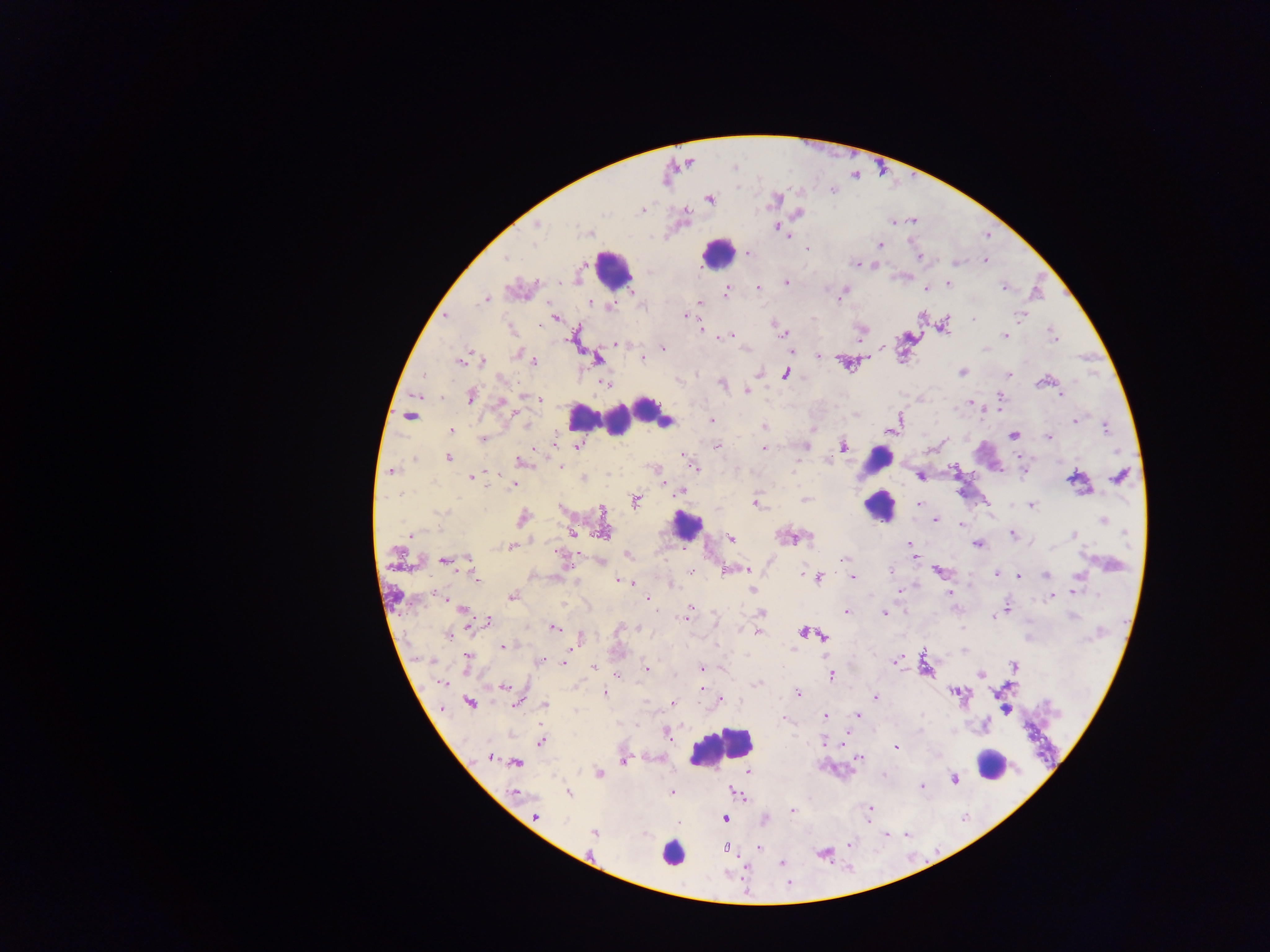
Approximate centers as {x, y} in pixels. Malaria parasite locations: {709, 199}, {774, 201}, {641, 211}, {798, 213}, {537, 225}, {778, 229}, {589, 233}, {880, 244}, {807, 248}, {748, 254}, {919, 257}, {506, 258}, {986, 260}, {856, 263}, {786, 283}, {949, 284}, {1003, 286}, {758, 288}, {926, 288}, {725, 291}, {841, 293}, {486, 300}, {701, 302}, {592, 303}, {611, 306}, {686, 315}, {1019, 316}, {554, 318}, {973, 319}, {944, 325}, {700, 329}, {778, 329}, {782, 333}, {1053, 334}, {729, 335}, {1005, 335}, {618, 344}, {882, 347}, {663, 349}, {985, 349}, {518, 354}, {819, 356}, {529, 358}, {642, 358}, {597, 359}, {481, 360}, {460, 361}, {534, 361}, {962, 372}, {758, 374}, {1009, 374}, {425, 375}, {786, 375}, {501, 379}, {1042, 381}, {605, 383}, {722, 384}, {748, 390}, {1061, 394}, {471, 396}, {532, 397}, {999, 397}, {539, 399}, {501, 402}, {971, 402}, {899, 418}, {713, 420}, {1076, 421}, {665, 423}, {896, 423}, {527, 424}, {764, 427}, {1105, 427}, {451, 430}, {1013, 435}, {483, 438}, {1049, 438}, {554, 442}, {718, 445}, {578, 446}, {805, 446}, {844, 447}, {764, 448}, {447, 458}, {522, 462}, {560, 466}, {694, 468}, {391, 471}, {471, 477}, {920, 477}, {1120, 477}, {583, 479}, {1073, 479}, {513, 485}, {678, 492}, {399, 494}, {805, 499}, {636, 501}, {757, 503}, {918, 504}, {1031, 505}, {440, 512}, {523, 517}, {935, 520}, {1103, 520}, {960, 524}, {603, 531}, {573, 532}, {1012, 533}, {1125, 533}, {410, 534}, {1074, 535}, {808, 537}, {731, 538}, {910, 543}, {977, 544}, {510, 546}, {627, 555}, {915, 556}, {844, 558}, {563, 559}, {445, 560}, {468, 560}, {600, 561}, {745, 568}, {691, 571}, {890, 571}, {726, 572}, {939, 572}, {996, 573}, {1000, 574}, {1045, 574}, {803, 575}, {1078, 576}, {819, 577}, {1019, 577}, {852, 578}, {477, 579}, {620, 581}, {630, 582}, {672, 586}, {752, 590}, {899, 591}, {1074, 592}, {950, 593}, {512, 596}, {1051, 597}, {648, 599}, {1005, 606}, {690, 608}, {462, 609}, {847, 611}, {762, 613}, {884, 613}, {688, 614}, {994, 616}, {488, 622}, {638, 627}, {554, 628}, {758, 633}, {803, 633}, {448, 634}, {817, 635}, {823, 636}, {503, 646}, {468, 660}, {542, 661}, {564, 662}, {897, 662}, {1014, 666}, {594, 667}, {647, 667}, {701, 668}, {831, 675}, {981, 675}, {617, 677}, {443, 683}, {758, 683}, {504, 688}, {701, 689}, {955, 692}, {604, 693}, {798, 694}, {876, 697}, {720, 699}, {517, 702}, {470, 703}, {672, 703}, {545, 704}, {857, 716}, {825, 717}, {783, 719}, {669, 736}, {541, 742}, {824, 742}, {897, 747}, {489, 757}, {858, 758}, {623, 761}, {516, 763}, {749, 771}, {599, 774}, {954, 780}, {922, 787}, {672, 792}, {513, 793}, {569, 793}, {735, 793}, {869, 809}, {792, 810}, {536, 817}, {725, 819}, {765, 820}, {594, 833}, {849, 843}, {725, 848}, {759, 849}, {782, 863}. Leukocyte locations: {717, 252}, {613, 268}, {645, 408}, {409, 413}, {629, 413}, {582, 416}, {617, 422}, {877, 461}, {879, 507}, {686, 525}, {721, 748}, {992, 764}, {672, 853}. Image is 1270×952 pixels. Sample from Ghana. One field of view. Mobile-phone photograph taken through the microscope. Thick blood film.